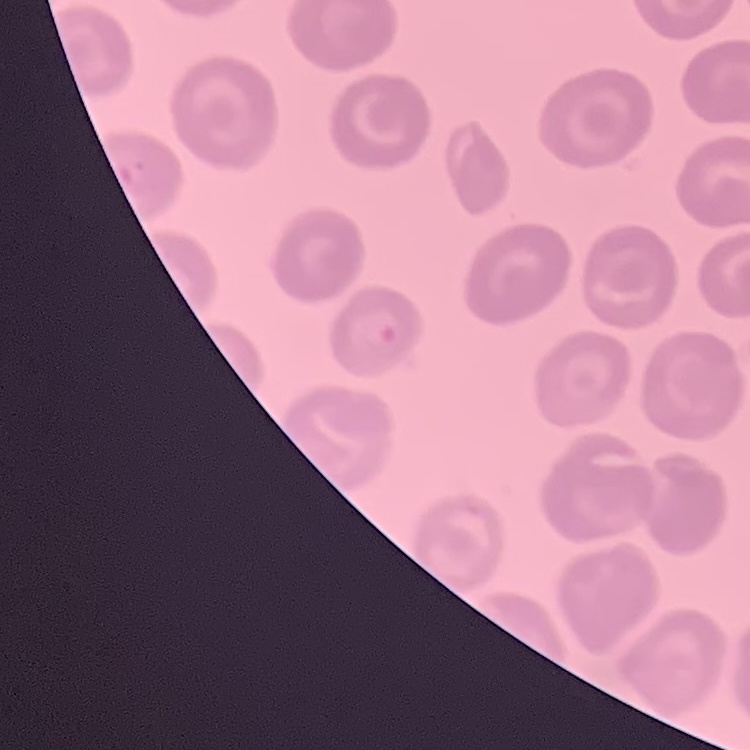

Summary:
  - Red blood cell morphology: no rouleaux formation
  - Stain: Field's or Giemsa
  - Preparation: thin blood film
  - Image type: square crop of a larger photomicrograph